Report the malaria status of this cell.
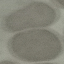

It is uninfected.

Cell patch, automatically extracted from a larger field of view and resized to 64 × 64 pixels. Photographed with a smartphone camera at the microscope eyepiece. Thin blood smear. Giemsa stain.